Locate every Plasmodium falciparum-infected red blood cell.
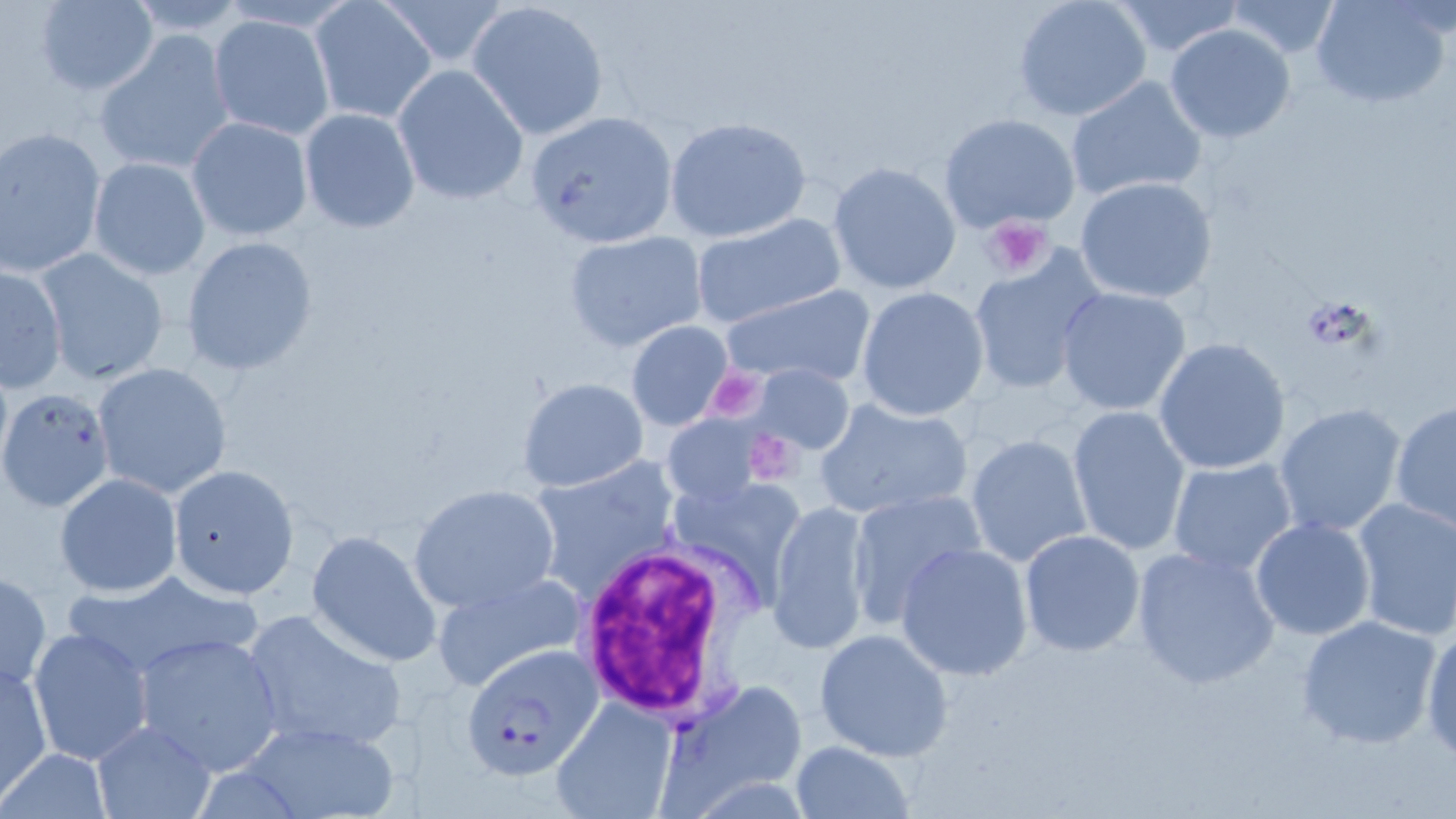
Approximate bounding boxes as named x1/y1/x2/y2 corners in pixels.
Plasmodium falciparum-infected red blood cells: (x1=462, y1=645, x2=602, y2=778), (x1=658, y1=679, x2=811, y2=812).

Summary:
  - Platelet locations: (x1=983, y1=217, x2=1055, y2=277), (x1=1297, y1=298, x2=1376, y2=353)
  - Uninfected red blood cell locations: (x1=376, y1=0, x2=512, y2=67), (x1=465, y1=0, x2=610, y2=142), (x1=1012, y1=0, x2=1150, y2=122), (x1=1221, y1=0, x2=1344, y2=61), (x1=1310, y1=0, x2=1452, y2=108), (x1=32, y1=1, x2=159, y2=95), (x1=308, y1=1, x2=438, y2=123), (x1=1109, y1=1, x2=1246, y2=58), (x1=208, y1=14, x2=336, y2=141), (x1=1163, y1=24, x2=1296, y2=145), (x1=95, y1=31, x2=235, y2=176), (x1=392, y1=65, x2=528, y2=206), (x1=1065, y1=75, x2=1207, y2=205), (x1=298, y1=108, x2=420, y2=233), (x1=525, y1=110, x2=680, y2=250), (x1=937, y1=113, x2=1079, y2=232), (x1=186, y1=116, x2=313, y2=241), (x1=664, y1=117, x2=811, y2=243), (x1=1, y1=127, x2=106, y2=276), (x1=88, y1=156, x2=211, y2=280), (x1=827, y1=162, x2=961, y2=294), (x1=1075, y1=176, x2=1217, y2=305), (x1=690, y1=214, x2=847, y2=329), (x1=565, y1=231, x2=709, y2=354), (x1=179, y1=235, x2=317, y2=376), (x1=33, y1=247, x2=170, y2=387), (x1=967, y1=251, x2=1104, y2=395), (x1=1, y1=264, x2=68, y2=392), (x1=719, y1=286, x2=876, y2=386), (x1=857, y1=287, x2=989, y2=420), (x1=1056, y1=288, x2=1192, y2=415), (x1=625, y1=320, x2=737, y2=431), (x1=1153, y1=337, x2=1291, y2=474), (x1=92, y1=362, x2=233, y2=498), (x1=752, y1=363, x2=855, y2=455), (x1=517, y1=377, x2=650, y2=493), (x1=0, y1=387, x2=117, y2=513), (x1=814, y1=397, x2=975, y2=521), (x1=1389, y1=400, x2=1455, y2=534), (x1=1273, y1=402, x2=1408, y2=540), (x1=1067, y1=406, x2=1190, y2=555), (x1=662, y1=410, x2=768, y2=509), (x1=965, y1=433, x2=1093, y2=567), (x1=1166, y1=457, x2=1297, y2=577), (x1=528, y1=458, x2=683, y2=600), (x1=167, y1=464, x2=299, y2=598), (x1=54, y1=474, x2=182, y2=595), (x1=664, y1=474, x2=812, y2=614), (x1=408, y1=484, x2=561, y2=613), (x1=846, y1=490, x2=990, y2=626), (x1=1348, y1=496, x2=1456, y2=640), (x1=768, y1=499, x2=875, y2=655), (x1=1249, y1=518, x2=1377, y2=641), (x1=305, y1=530, x2=442, y2=667), (x1=1019, y1=530, x2=1146, y2=658), (x1=896, y1=543, x2=1034, y2=681), (x1=1130, y1=544, x2=1283, y2=690), (x1=0, y1=568, x2=50, y2=692), (x1=60, y1=568, x2=264, y2=685), (x1=433, y1=570, x2=590, y2=694), (x1=238, y1=608, x2=410, y2=754), (x1=1296, y1=614, x2=1442, y2=749), (x1=1419, y1=621, x2=1456, y2=764), (x1=28, y1=628, x2=153, y2=765), (x1=813, y1=628, x2=952, y2=760), (x1=130, y1=631, x2=284, y2=776), (x1=0, y1=662, x2=51, y2=803), (x1=551, y1=695, x2=679, y2=818), (x1=232, y1=719, x2=400, y2=819), (x1=90, y1=720, x2=217, y2=818), (x1=790, y1=740, x2=913, y2=819), (x1=0, y1=749, x2=111, y2=818)
  - White blood cell locations: (x1=573, y1=541, x2=745, y2=722)
  - Slide-level diagnosis: Plasmodium falciparum
  - Preparation: thin blood film
  - Image size: 1456×819 pixels
  - Field of view: single
  - Stain: May-Grünwald-Giemsa
  - Magnification: 1000x
  - Modality: light microscopy